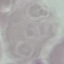

Result: negative for malaria parasites. Photographed with a smartphone camera at the microscope eyepiece. Giemsa-stained preparation. Cell patch, automatically extracted from a larger field of view and resized to 64 × 64 pixels. Thin blood smear.